Locate and identify every blood parasite.
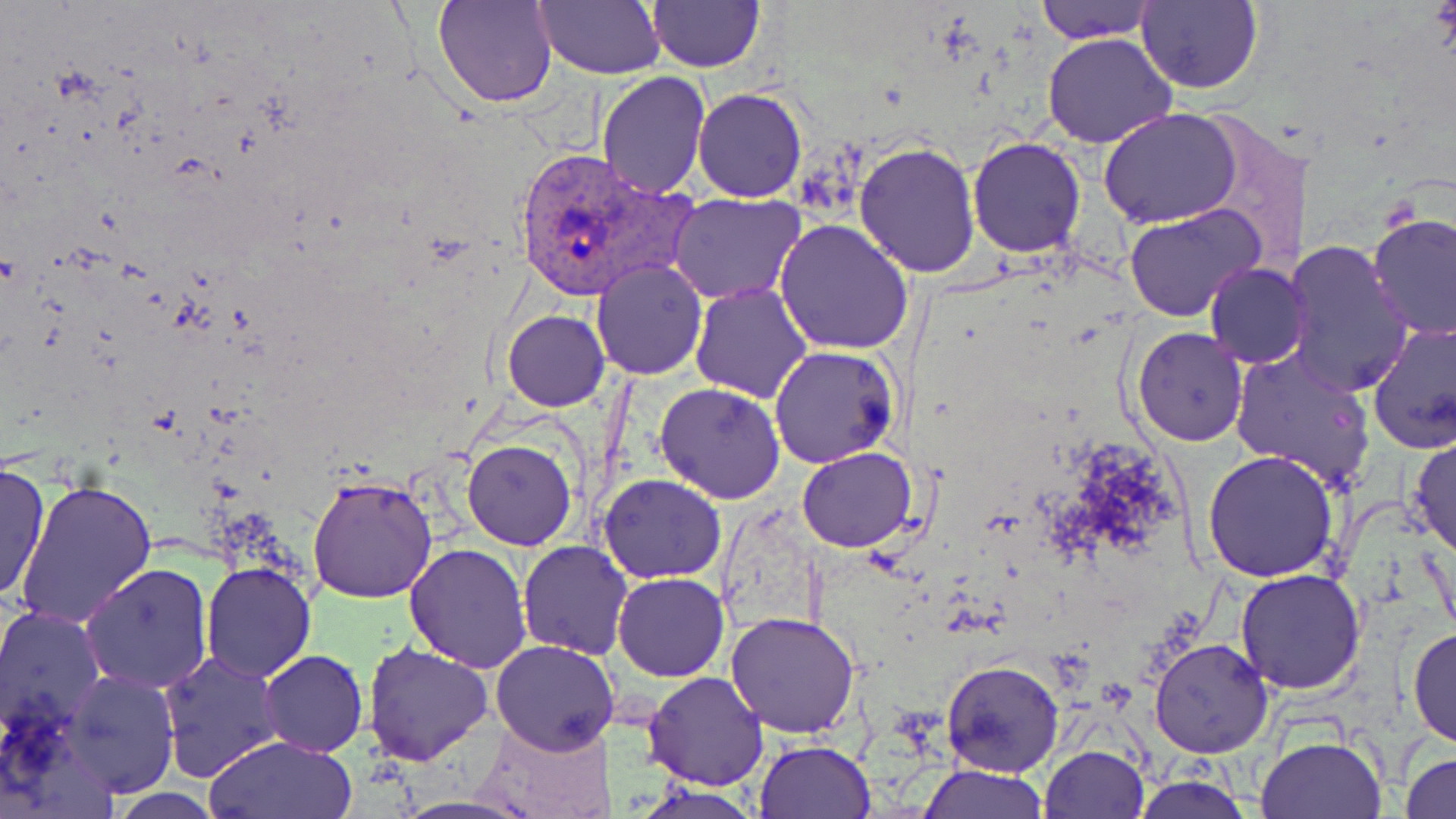

Approximate bounding boxes as (x1,y1)-(x2,y2) corner pairs in pixels.
Plasmodium vivax-infected red blood cells: (510,146)-(691,300).
No Plasmodium falciparum, Plasmodium ovale, Plasmodium malariae, Babesia divergens, or Trypanosoma brucei observed.

slide-level diagnosis = Plasmodium vivax
stain = May-Grünwald-Giemsa
image size = 1456×819 pixels
uninfected red blood cell locations = approximate bounding boxes as (x1,y1)-(x2,y2) corner pairs in pixels: (433,0)-(558,108), (536,0)-(664,79), (648,1)-(763,71), (1034,1)-(1159,44), (1135,1)-(1262,93), (1043,33)-(1176,148), (596,70)-(711,198), (693,89)-(808,202), (1100,109)-(1243,228), (968,136)-(1087,257), (854,141)-(980,280), (670,195)-(806,305), (1122,203)-(1266,321), (1367,212)-(1455,338), (775,220)-(914,356), (1282,239)-(1414,398), (591,258)-(707,380), (1204,262)-(1311,367), (690,281)-(814,402), (503,310)-(608,410), (1367,320)-(1456,453), (1132,327)-(1249,446), (769,345)-(898,468), (1230,348)-(1376,490), (655,381)-(785,503), (1409,432)-(1455,557), (461,439)-(576,551), (797,447)-(918,554), (1203,450)-(1339,581), (0,461)-(49,605), (598,473)-(727,583), (309,475)-(438,605), (13,479)-(158,629), (518,540)-(632,659), (404,541)-(533,672), (202,562)-(316,682), (80,563)-(210,692), (1235,569)-(1366,695), (612,572)-(729,682), (0,605)-(105,736), (725,611)-(861,738), (1406,626)-(1456,750), (1148,636)-(1274,757), (491,638)-(620,754), (362,641)-(493,765), (157,650)-(285,783), (261,650)-(367,757), (941,660)-(1064,778), (63,669)-(178,797), (644,672)-(767,790), (475,713)-(619,819), (202,733)-(357,819), (1256,735)-(1387,819), (753,740)-(874,819), (1039,745)-(1149,819), (1401,750)-(1456,819), (916,764)-(1049,819), (1128,770)-(1256,818)
field of view = one of a larger specimen
preparation = thin blood smear
modality = light microscopy
magnification = 1000x